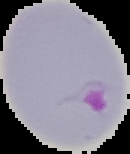

Segmented cell region on a black background. From a thin blood film. Result: Plasmodium parasites detected. Image is 130×154 pixels.